Locate every blood parasite and identify its species.
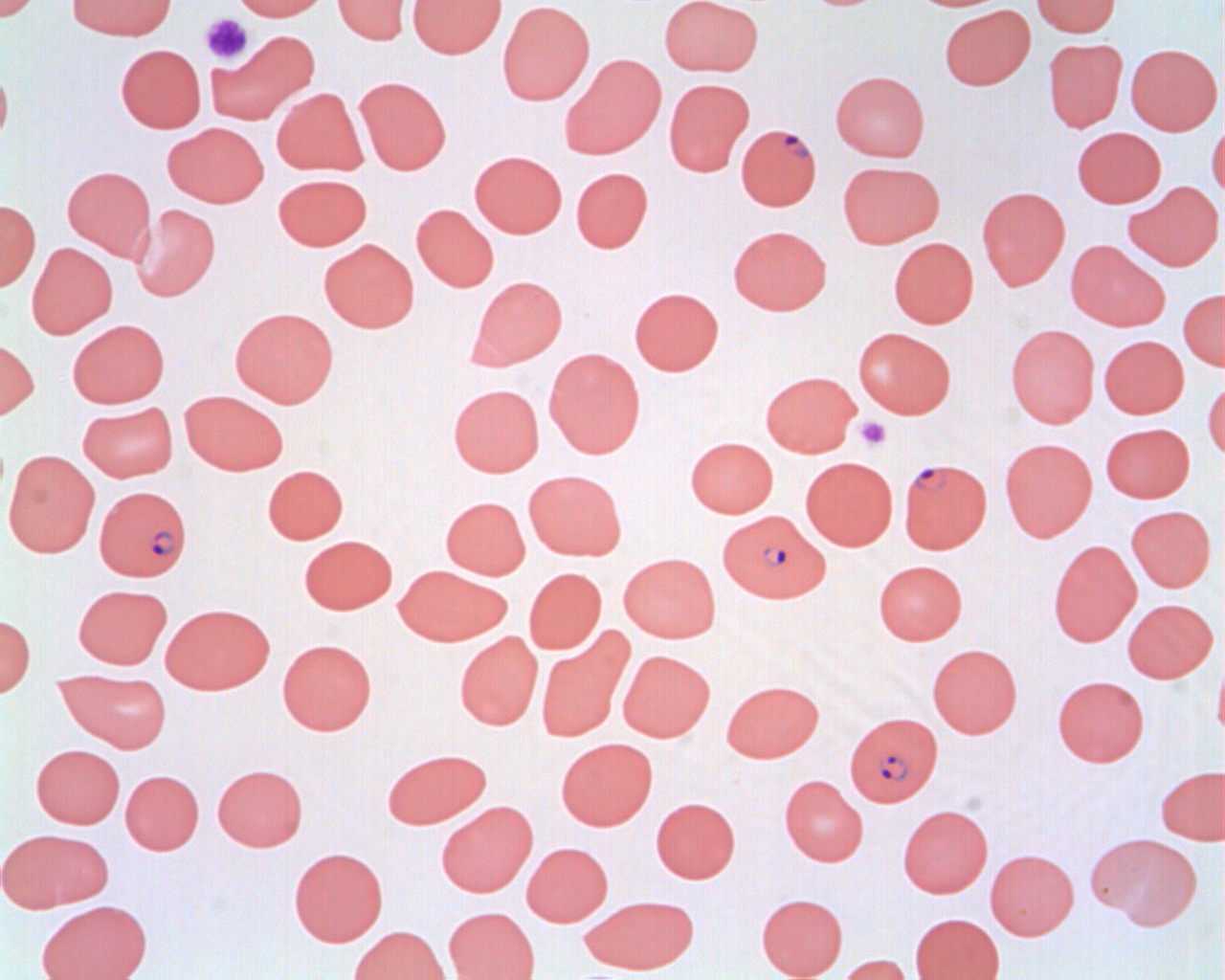

Approximate bounding boxes as named x1/y1/x2/y2 corners in pixels.
Plasmodium falciparum-infected red blood cells: (x1=736, y1=123, x2=821, y2=210), (x1=902, y1=459, x2=994, y2=555), (x1=98, y1=487, x2=196, y2=583), (x1=718, y1=510, x2=829, y2=602), (x1=845, y1=711, x2=942, y2=805).
No Plasmodium ovale, Plasmodium malariae, Plasmodium vivax, Babesia divergens, or Trypanosoma brucei observed.

Uninfected red blood cell locations: (x1=0, y1=0, x2=44, y2=21), (x1=67, y1=0, x2=176, y2=40), (x1=229, y1=0, x2=332, y2=21), (x1=333, y1=0, x2=415, y2=45), (x1=408, y1=0, x2=506, y2=58), (x1=659, y1=0, x2=763, y2=76), (x1=1031, y1=0, x2=1120, y2=37), (x1=497, y1=1, x2=595, y2=104), (x1=939, y1=5, x2=1035, y2=90), (x1=205, y1=30, x2=319, y2=124), (x1=1043, y1=38, x2=1127, y2=133), (x1=116, y1=44, x2=206, y2=132), (x1=1126, y1=44, x2=1222, y2=135), (x1=561, y1=54, x2=666, y2=159), (x1=0, y1=64, x2=13, y2=151), (x1=830, y1=70, x2=930, y2=162), (x1=354, y1=76, x2=451, y2=175), (x1=664, y1=78, x2=754, y2=175), (x1=272, y1=87, x2=368, y2=176), (x1=1208, y1=116, x2=1225, y2=205), (x1=163, y1=122, x2=268, y2=207), (x1=1072, y1=127, x2=1166, y2=207), (x1=470, y1=150, x2=567, y2=237), (x1=837, y1=161, x2=944, y2=248), (x1=62, y1=165, x2=156, y2=261), (x1=571, y1=167, x2=653, y2=252), (x1=274, y1=173, x2=372, y2=250), (x1=1124, y1=181, x2=1223, y2=271), (x1=976, y1=186, x2=1070, y2=289), (x1=0, y1=199, x2=40, y2=291), (x1=132, y1=204, x2=220, y2=301), (x1=411, y1=204, x2=499, y2=292), (x1=728, y1=225, x2=831, y2=314), (x1=889, y1=237, x2=978, y2=328), (x1=319, y1=239, x2=419, y2=332), (x1=1066, y1=240, x2=1169, y2=331), (x1=26, y1=242, x2=117, y2=338), (x1=468, y1=276, x2=567, y2=369), (x1=629, y1=287, x2=723, y2=375), (x1=1178, y1=288, x2=1225, y2=371), (x1=230, y1=307, x2=338, y2=406), (x1=67, y1=319, x2=169, y2=407), (x1=1006, y1=324, x2=1099, y2=427), (x1=853, y1=327, x2=957, y2=418), (x1=0, y1=335, x2=39, y2=421), (x1=1099, y1=335, x2=1188, y2=418), (x1=544, y1=348, x2=645, y2=458), (x1=761, y1=371, x2=861, y2=457), (x1=1202, y1=378, x2=1225, y2=460), (x1=448, y1=384, x2=544, y2=476), (x1=180, y1=390, x2=288, y2=475), (x1=77, y1=401, x2=178, y2=482), (x1=1100, y1=422, x2=1195, y2=502), (x1=686, y1=437, x2=778, y2=518), (x1=1000, y1=437, x2=1097, y2=541), (x1=4, y1=449, x2=100, y2=557), (x1=801, y1=456, x2=898, y2=550), (x1=263, y1=464, x2=348, y2=543), (x1=524, y1=470, x2=627, y2=560), (x1=441, y1=496, x2=530, y2=578), (x1=1127, y1=505, x2=1215, y2=592), (x1=299, y1=534, x2=397, y2=614), (x1=1048, y1=540, x2=1141, y2=647), (x1=619, y1=553, x2=721, y2=642), (x1=873, y1=560, x2=967, y2=644), (x1=394, y1=564, x2=512, y2=645), (x1=524, y1=567, x2=606, y2=654), (x1=73, y1=584, x2=171, y2=668), (x1=1122, y1=598, x2=1217, y2=683), (x1=161, y1=603, x2=274, y2=693), (x1=0, y1=614, x2=35, y2=697), (x1=536, y1=629, x2=632, y2=742), (x1=455, y1=631, x2=543, y2=729), (x1=278, y1=639, x2=377, y2=735), (x1=927, y1=643, x2=1022, y2=737), (x1=1213, y1=650, x2=1225, y2=742), (x1=623, y1=652, x2=719, y2=744), (x1=55, y1=670, x2=171, y2=752), (x1=1052, y1=675, x2=1149, y2=766), (x1=721, y1=679, x2=824, y2=762), (x1=556, y1=737, x2=657, y2=830), (x1=31, y1=744, x2=125, y2=828), (x1=381, y1=747, x2=491, y2=829), (x1=213, y1=764, x2=308, y2=851), (x1=1156, y1=766, x2=1224, y2=844), (x1=121, y1=770, x2=203, y2=854), (x1=780, y1=774, x2=868, y2=866), (x1=651, y1=797, x2=740, y2=883), (x1=436, y1=800, x2=537, y2=897), (x1=898, y1=804, x2=993, y2=898), (x1=0, y1=828, x2=112, y2=913), (x1=1090, y1=832, x2=1202, y2=931), (x1=522, y1=842, x2=612, y2=926), (x1=288, y1=847, x2=388, y2=946), (x1=985, y1=849, x2=1078, y2=940), (x1=756, y1=893, x2=848, y2=979), (x1=581, y1=894, x2=699, y2=974), (x1=36, y1=900, x2=152, y2=980), (x1=444, y1=906, x2=540, y2=980), (x1=910, y1=913, x2=1004, y2=980), (x1=347, y1=925, x2=451, y2=980), (x1=835, y1=954, x2=913, y2=980). Platelet locations: (x1=200, y1=13, x2=253, y2=65), (x1=854, y1=416, x2=893, y2=451). Slide-level diagnosis: Plasmodium falciparum. Image is 1225×980 pixels. Thin blood smear. Single field of view. Captured at 1000x magnification. Light microscopy.